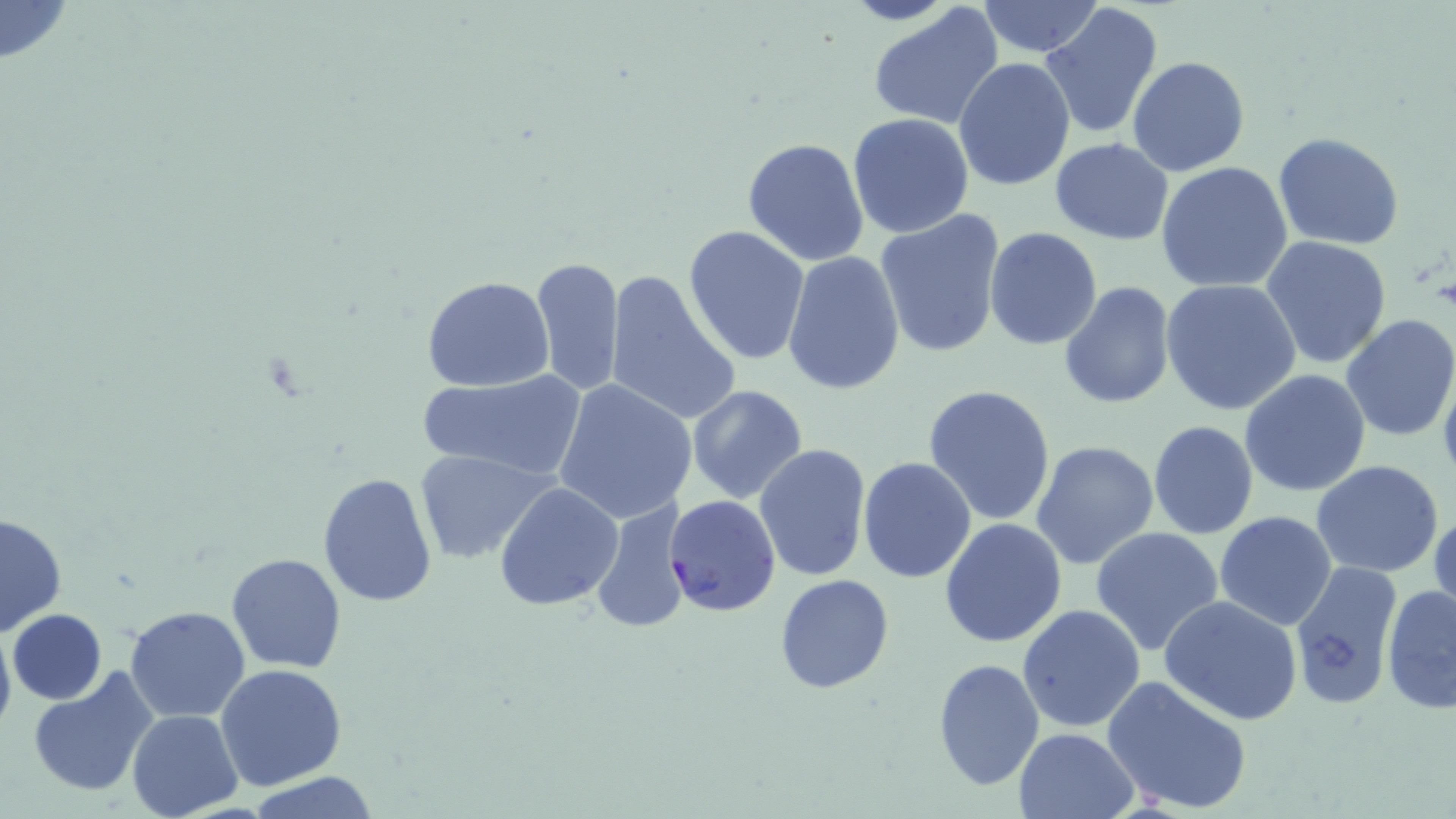

Summary:
  - Coordinate format: approximate bounding boxes as [x1, y1, x2, y2] in pixels
  - Plasmodium falciparum-infected red blood cell locations: [664, 494, 781, 618]
  - Uninfected red blood cell locations: [0, 0, 71, 62], [975, 0, 1104, 57], [1040, 3, 1165, 141], [866, 4, 1007, 133], [1127, 56, 1250, 176], [953, 58, 1075, 193], [847, 113, 976, 240], [1272, 133, 1404, 250], [741, 137, 871, 268], [1048, 138, 1174, 245], [1156, 161, 1293, 292], [875, 210, 1005, 359], [684, 225, 812, 365], [984, 227, 1102, 350], [1262, 235, 1392, 367], [781, 250, 908, 395], [531, 256, 625, 397], [603, 268, 741, 427], [422, 276, 555, 392], [1159, 278, 1302, 415], [1059, 283, 1175, 410], [1339, 314, 1456, 442], [1437, 361, 1456, 490], [415, 369, 586, 482], [1240, 370, 1372, 497], [554, 381, 698, 524], [923, 383, 1057, 526], [685, 386, 808, 503], [1147, 419, 1258, 540], [1031, 441, 1161, 572], [755, 443, 871, 582], [414, 449, 555, 563], [858, 456, 978, 584], [1311, 460, 1444, 579], [317, 472, 438, 608], [494, 482, 623, 611], [591, 499, 693, 635], [1429, 506, 1455, 625], [1215, 511, 1338, 630], [1, 513, 67, 637], [940, 517, 1068, 649], [1089, 526, 1225, 655], [225, 553, 347, 674], [1287, 560, 1402, 710], [774, 573, 893, 693], [1381, 584, 1456, 713], [1159, 594, 1303, 724], [1018, 604, 1146, 733], [126, 606, 252, 721], [8, 609, 106, 704], [0, 616, 16, 745], [932, 657, 1045, 791], [215, 665, 349, 791], [28, 669, 158, 800], [1101, 674, 1253, 814], [127, 710, 243, 819], [1013, 727, 1139, 818], [245, 772, 384, 818]
  - Slide-level diagnosis: Plasmodium falciparum
  - Image size: 1456×819 pixels
  - Field of view: single
  - Modality: optical microscopy
  - Magnification: 1000x
  - Preparation: thin blood smear
  - Stain: May-Grünwald-Giemsa